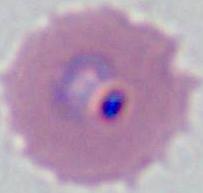

identification: Plasmodium
modality: photomicrograph
magnification: 400x or 1000x